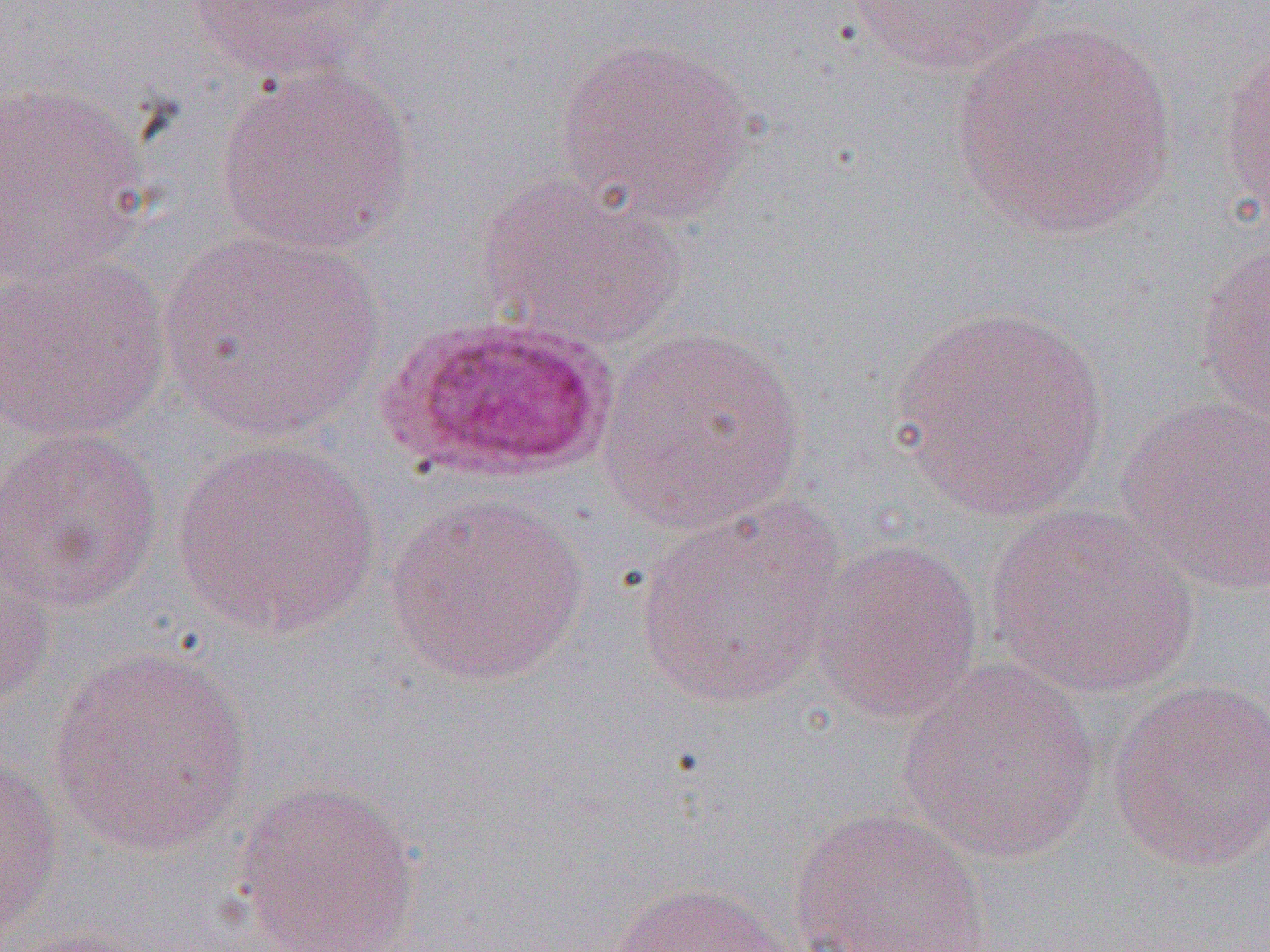
Approximate bounding boxes as [x1, y1, x2, y2] in pixels. Plasmodium ovale-infected red blood cell locations: [378, 312, 621, 483]. Uninfected red blood cell locations: [845, 0, 1050, 76], [182, 1, 396, 82], [949, 22, 1180, 243], [553, 36, 757, 225], [1218, 38, 1270, 227], [215, 64, 416, 254], [0, 81, 153, 288], [476, 173, 687, 352], [158, 229, 384, 442], [1196, 238, 1270, 431], [0, 254, 172, 445], [889, 304, 1113, 522], [600, 325, 808, 535], [1114, 396, 1270, 596], [0, 425, 165, 613], [169, 436, 383, 638], [384, 491, 590, 686], [631, 500, 848, 711], [984, 505, 1202, 699], [808, 537, 984, 725], [0, 546, 57, 712], [46, 645, 256, 857], [897, 659, 1102, 863], [1105, 677, 1270, 873], [0, 749, 63, 937], [231, 779, 422, 952], [790, 807, 992, 952], [609, 880, 798, 952], [6, 925, 160, 952]. Slide-level diagnosis: Plasmodium ovale. Image is 1270×952 pixels. One field of a larger specimen. Thin blood film. Light microscopy. Captured at 1000x magnification.